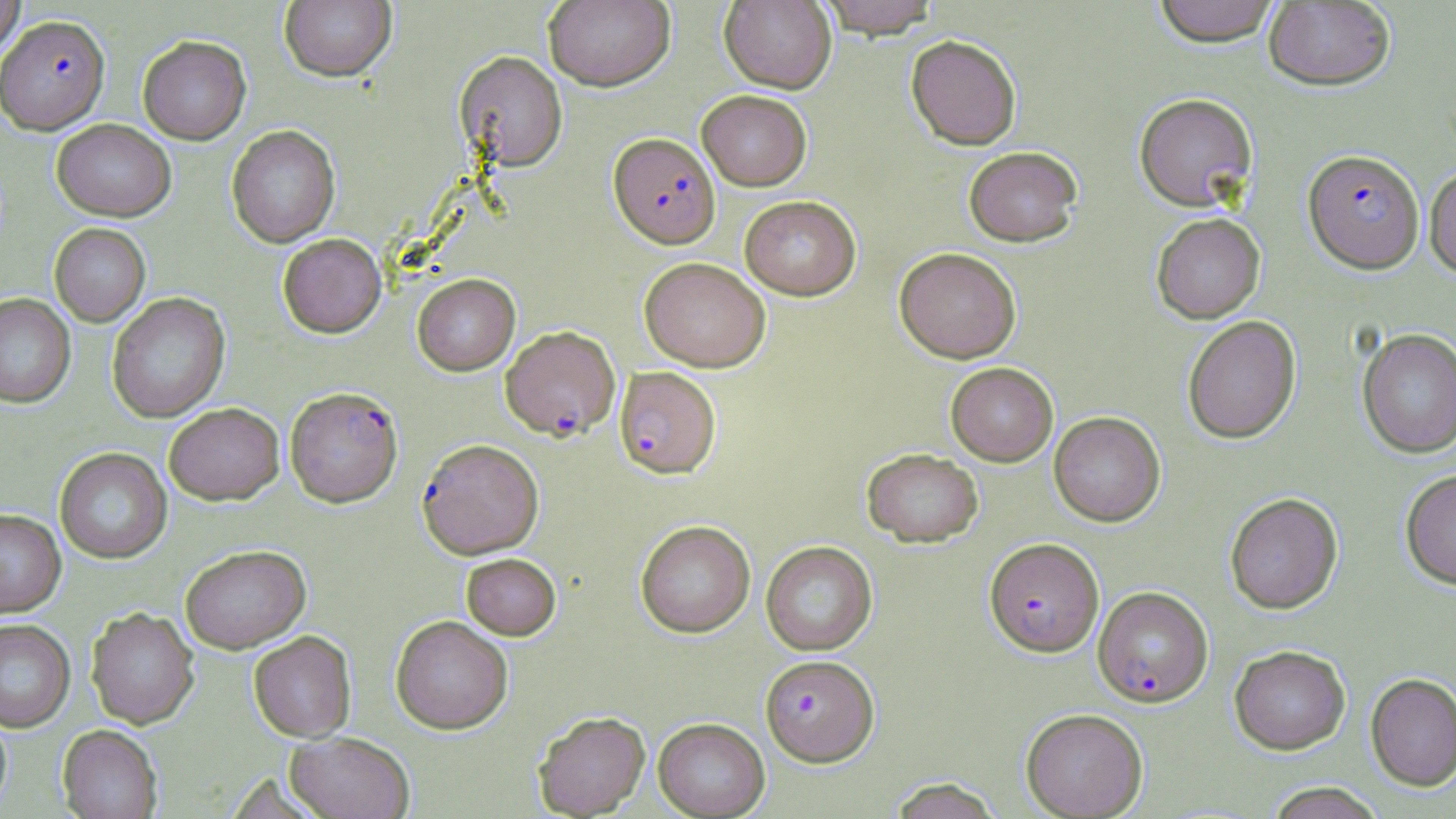 Approximate bounding boxes as [x1, y1, x2, y2] in pixels. Uninfected red blood cell locations: [0, 0, 26, 60], [543, 0, 675, 91], [720, 0, 837, 94], [816, 0, 941, 39], [1152, 0, 1280, 48], [279, 1, 397, 82], [1264, 1, 1395, 91], [905, 34, 1022, 150], [137, 35, 251, 145], [455, 51, 567, 171], [697, 89, 812, 191], [1134, 93, 1257, 212], [51, 118, 176, 221], [226, 125, 340, 248], [963, 146, 1083, 247], [1425, 165, 1456, 280], [740, 195, 861, 300], [1151, 213, 1265, 324], [49, 223, 150, 327], [277, 233, 387, 338], [894, 247, 1021, 363], [639, 257, 770, 372], [412, 273, 520, 376], [107, 293, 231, 423], [0, 294, 76, 408], [1182, 315, 1302, 444], [1356, 327, 1456, 459], [946, 362, 1058, 466], [164, 403, 285, 505], [1049, 411, 1165, 526], [54, 448, 172, 563], [862, 448, 983, 547], [1400, 469, 1456, 590], [1225, 493, 1343, 614], [0, 509, 66, 617], [635, 520, 755, 637], [761, 540, 878, 655], [180, 544, 311, 654], [461, 553, 561, 639], [86, 608, 199, 730], [391, 615, 513, 734], [0, 620, 75, 732], [248, 631, 356, 742], [1229, 644, 1350, 755], [1366, 673, 1456, 792], [1020, 708, 1148, 818], [0, 710, 12, 815], [533, 711, 650, 817], [653, 717, 770, 818], [58, 725, 162, 819], [285, 732, 415, 819], [888, 777, 1003, 819], [1265, 783, 1385, 819]. Plasmodium falciparum-infected red blood cell locations: [0, 15, 110, 135], [609, 133, 720, 248], [1303, 149, 1424, 273], [500, 326, 620, 442], [615, 367, 721, 479], [285, 386, 403, 508], [417, 438, 544, 559], [984, 537, 1104, 657], [1092, 585, 1213, 707], [760, 655, 879, 766]. Slide-level diagnosis: Plasmodium falciparum. May-Grünwald-Giemsa-stained preparation. Image is 1456×819 pixels. Optical microscopy. Captured at 1000x magnification. One field of a larger specimen. Thin blood film.